State the preparation type.
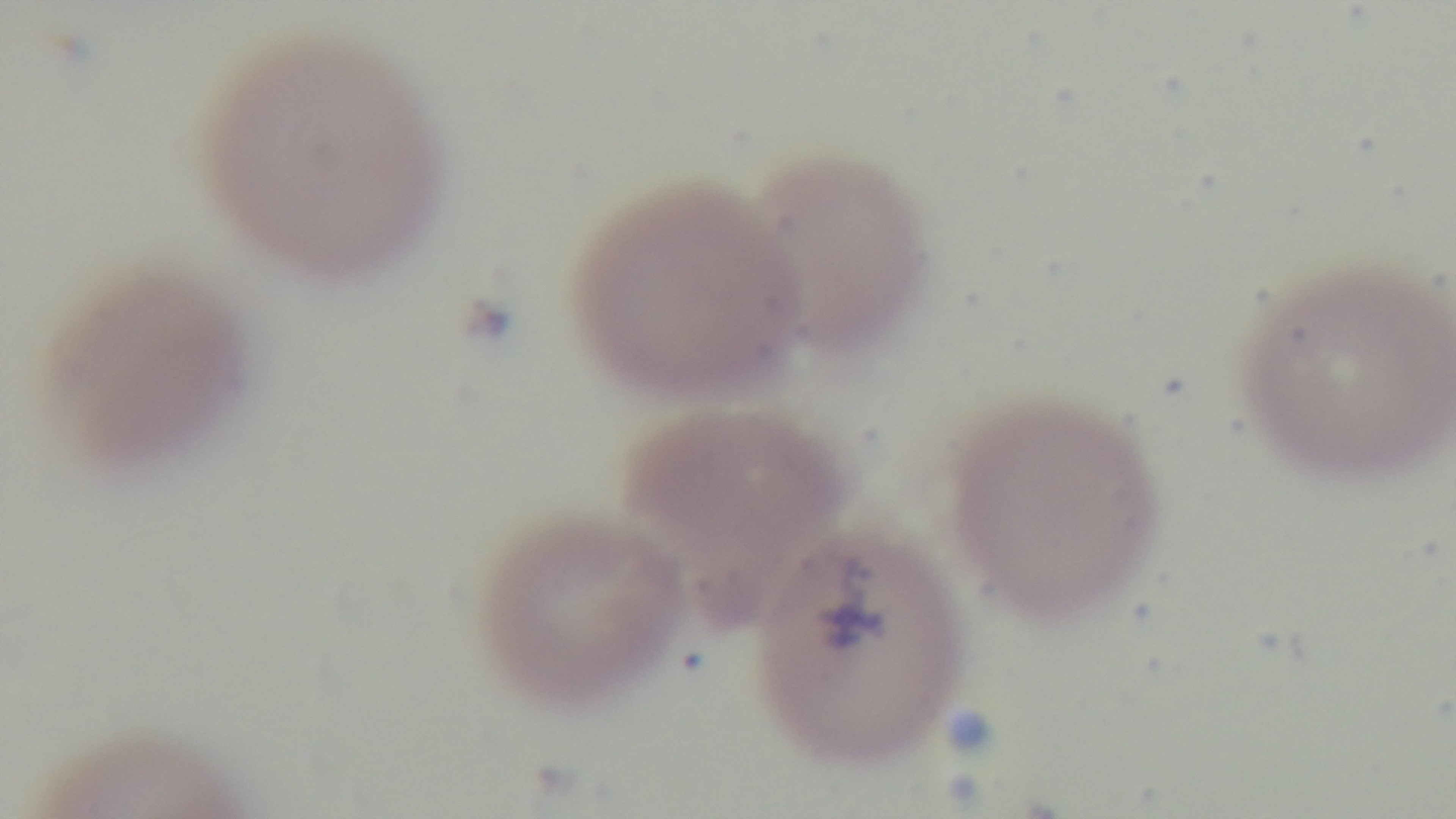

It is a thin blood film.

capture = mounted 4K digital camera
stain = Giemsa
malaria status = positive
modality = light microscopy
objective = 100x oil immersion
field of view = one from the slide